Classify this cell by malaria status.
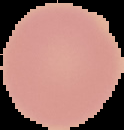

It is uninfected.

Image is 124×130 pixels. Segmented cell region on a black background. From a thin blood film.